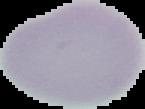
preparation = thin blood smear
image size = 145×109 pixels
image type = segmented cell region on a black background
result = no malaria parasites seen